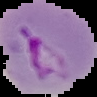
Summary:
  - Preparation: thin blood smear
  - Image type: cell region segmented out of the field of view; surrounding area masked to black
  - Image size: 97×97 pixels
  - Result: Plasmodium parasites identified